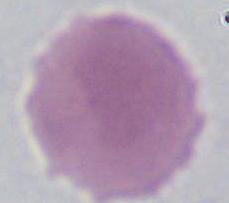

magnification = 1000x
modality = photomicrograph
identification = erythrocyte